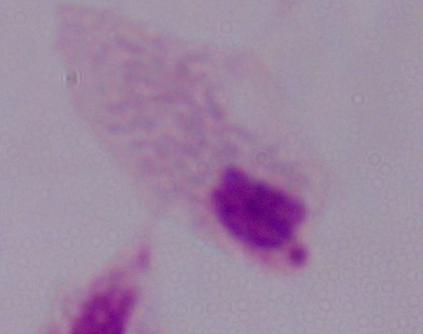

identification = trichomonad
modality = photomicrograph
magnification = 1000x